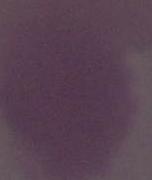

An erythrocyte is shown. Micrograph. Captured at 1000x magnification.